Classify this cell by malaria status.
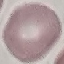
Uninfected.

Giemsa-stained preparation. Thin blood film. Acquired by smartphone through the microscope eyepiece. Cell patch, automatically extracted from a larger field of view and resized to 64 × 64 pixels.